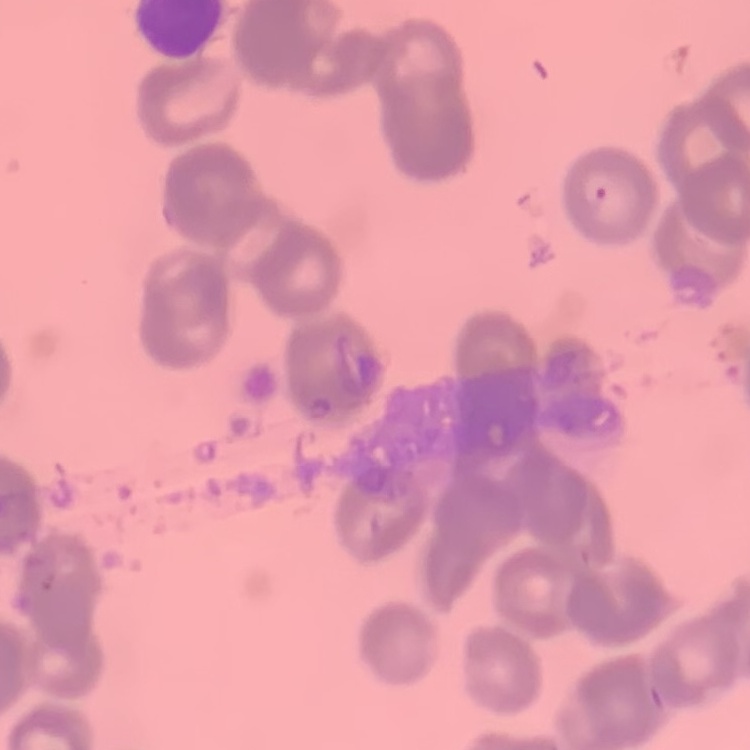

{
  "erythrocyte_morphology": "rouleaux formation",
  "preparation": "thin peripheral smear",
  "image_type": "square crop of a larger photomicrograph",
  "stain": "Field's or Giemsa"
}